Locate and identify every blood parasite.
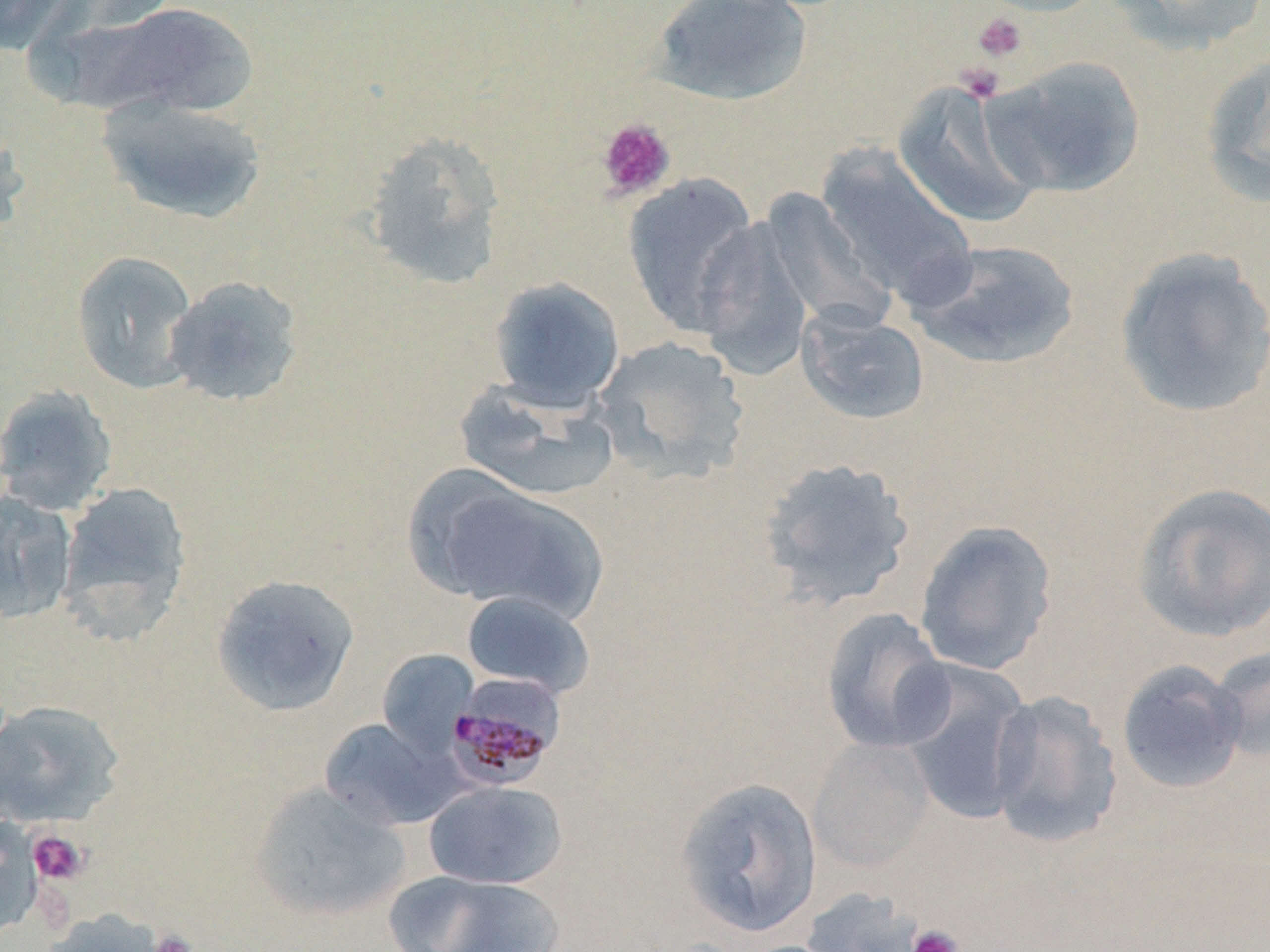
Approximate bounding boxes as [x1, y1, x2, y2] in pixels.
Plasmodium malariae-infected red blood cells: [446, 677, 564, 792].
No Plasmodium falciparum, Plasmodium ovale, Plasmodium vivax, Babesia divergens, or Trypanosoma brucei observed.

slide_level_diagnosis: Plasmodium malariae
platelet_locations: 'approximate bounding boxes as [x1, y1, x2, y2] in pixels: [972, 12, 1029, 64], [955, 63, 1005, 103], [596, 118, 676, 202], [28, 830, 88, 885], [907, 925, 963, 952], [149, 928, 199, 952]'
magnification: 1000x
image_size: 1270×952 pixels
stain: May-Grünwald-Giemsa
preparation: thin blood film
field_of_view: single
uninfected_red_blood_cell_locations: 'approximate bounding boxes as [x1, y1, x2, y2] in pixels: [0, 0, 78, 55], [973, 0, 1109, 17], [1102, 0, 1269, 54], [80, 1, 258, 121], [648, 1, 814, 107], [1201, 54, 1270, 207], [981, 57, 1146, 197], [892, 79, 1046, 229], [97, 95, 268, 224], [0, 118, 31, 239], [362, 130, 508, 291], [815, 144, 978, 308], [621, 173, 762, 334], [760, 187, 894, 334], [692, 216, 815, 377], [907, 238, 1081, 370], [1114, 248, 1270, 419], [70, 250, 199, 393], [162, 274, 304, 407], [488, 276, 626, 410], [796, 305, 930, 426], [592, 335, 751, 484], [454, 380, 619, 503], [0, 384, 118, 515], [757, 456, 916, 611], [402, 465, 541, 600], [57, 480, 193, 643], [1131, 481, 1270, 644], [439, 483, 606, 622], [0, 491, 78, 624], [913, 519, 1058, 675], [211, 573, 360, 716], [461, 590, 595, 698], [820, 607, 954, 753], [1208, 644, 1270, 763], [377, 649, 479, 755], [1115, 659, 1248, 794], [897, 661, 1035, 826], [986, 688, 1124, 850], [0, 699, 125, 827], [318, 717, 462, 830], [808, 737, 934, 871], [674, 776, 823, 938], [424, 781, 568, 889], [248, 782, 411, 922], [1, 818, 44, 939], [384, 869, 565, 952], [799, 887, 928, 952], [39, 908, 171, 952]'
modality: optical microscopy